Comment on the morphology of the red blood cells.
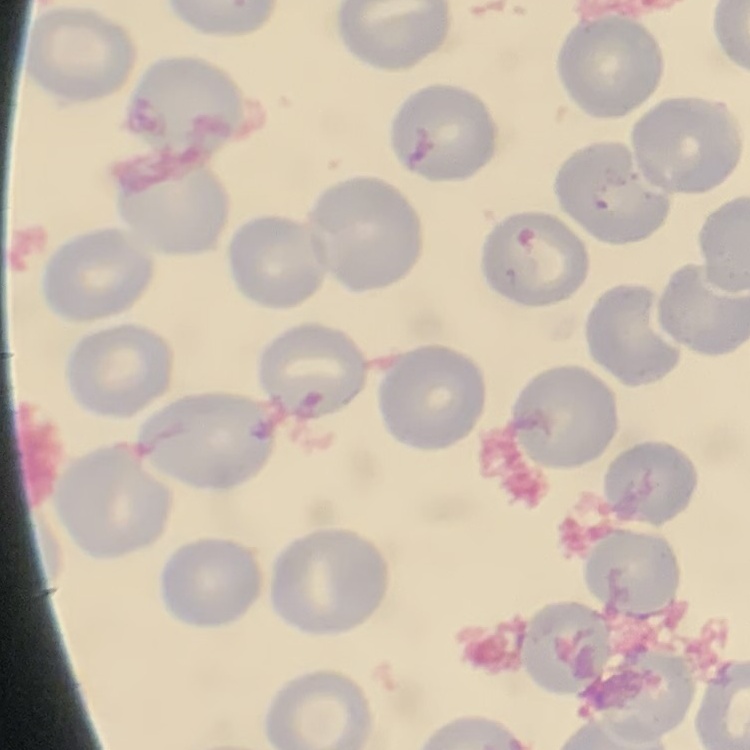
No rouleaux formation.

preparation = thin peripheral smear
image type = square crop of a larger photomicrograph
stain = Field's or Giemsa